Name the cell type shown.
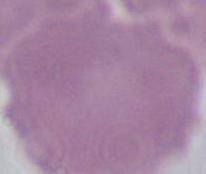

This is an erythrocyte.

Photomicrograph. Captured at 1000x magnification.